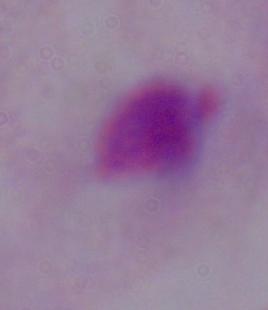

A trichomonad is shown. 1000x magnification. Photomicrograph.